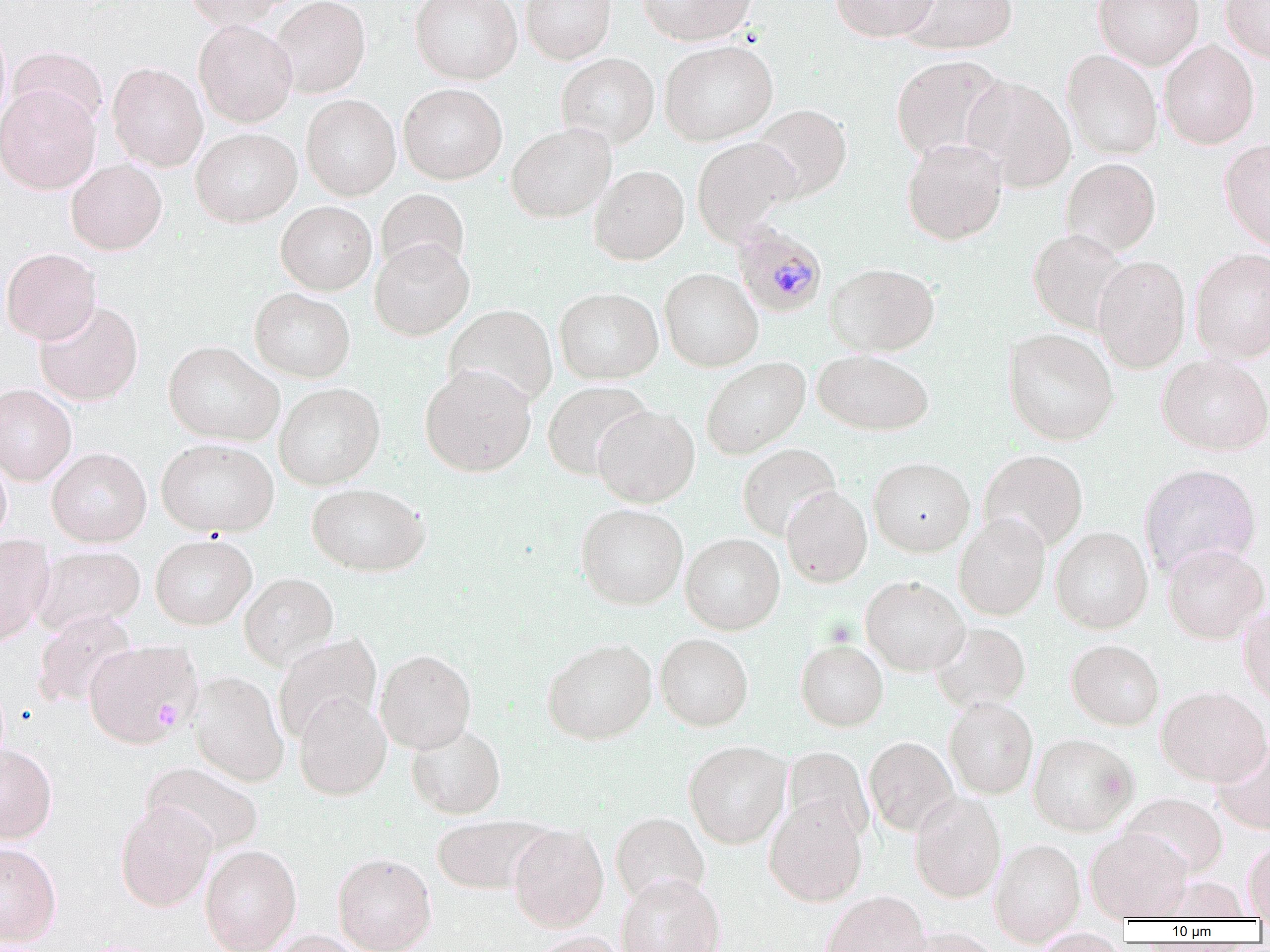

Approximate bounding boxes as (x1,y1)-(x2,y2) corner pairs in pixels. Plasmodium malariae-infected red blood cell locations: (731,221)-(828,319). Platelet locations: (156,700)-(182,732). Uninfected red blood cell locations: (184,0)-(297,28), (270,0)-(371,98), (410,0)-(522,84), (520,0)-(616,63), (638,0)-(758,45), (831,0)-(939,42), (1093,0)-(1204,69), (1220,0)-(1270,63), (898,1)-(1018,54), (194,19)-(297,127), (0,23)-(11,127), (659,39)-(778,146), (1159,39)-(1260,149), (9,47)-(109,131), (1061,49)-(1162,160), (556,52)-(659,147), (891,54)-(1007,162), (107,62)-(208,171), (962,75)-(1076,192), (398,83)-(507,185), (0,85)-(100,194), (301,94)-(401,201), (751,104)-(851,202), (506,123)-(616,222), (191,128)-(302,227), (692,137)-(799,242), (902,138)-(1008,245), (1219,138)-(1270,250), (1061,157)-(1161,256), (66,159)-(166,255), (589,165)-(689,265), (376,188)-(469,277), (276,201)-(377,295), (1028,229)-(1131,334), (370,238)-(474,340), (1,247)-(101,344), (1189,248)-(1270,363), (1092,255)-(1190,373), (825,262)-(940,356), (659,268)-(763,372), (250,287)-(355,382), (554,287)-(663,384), (34,301)-(143,406), (444,304)-(557,408), (1003,329)-(1119,445), (163,340)-(284,446), (813,349)-(933,436), (1157,353)-(1270,456), (701,356)-(810,458), (420,363)-(536,476), (542,380)-(651,479), (274,382)-(385,489), (0,384)-(77,485), (592,405)-(700,507), (156,437)-(279,537), (737,443)-(841,540), (47,447)-(151,547), (979,449)-(1088,553), (0,455)-(11,546), (868,456)-(975,556), (1139,464)-(1261,578), (307,482)-(431,576), (782,486)-(872,587), (575,503)-(688,609), (953,513)-(1051,620), (1050,526)-(1153,633), (681,532)-(785,634), (0,534)-(56,645), (150,535)-(256,629), (1162,542)-(1269,643), (32,544)-(145,635), (240,572)-(338,670), (861,576)-(970,676), (1237,602)-(1270,705), (32,609)-(138,709), (930,622)-(1031,713), (272,632)-(382,745), (655,632)-(754,731), (83,638)-(202,749), (542,638)-(657,744), (795,639)-(888,731), (1067,639)-(1164,730), (375,649)-(476,754), (188,671)-(288,787), (1157,685)-(1270,786), (293,693)-(392,800), (944,697)-(1038,798), (406,722)-(506,819), (1028,733)-(1138,836), (864,736)-(959,836), (1213,740)-(1270,834), (684,741)-(791,848), (0,743)-(57,843), (782,746)-(874,844), (142,761)-(264,856), (909,791)-(1006,903), (1119,792)-(1228,880), (764,797)-(868,906), (115,801)-(217,912), (611,812)-(710,906), (430,815)-(551,894), (509,823)-(609,932), (1086,828)-(1192,921), (989,838)-(1086,946), (1244,840)-(1270,919), (0,842)-(61,946), (200,844)-(302,952), (332,852)-(437,952), (616,873)-(725,952), (821,890)-(932,952), (903,927)-(1005,952), (1030,928)-(1128,952), (265,930)-(366,952), (526,931)-(631,952). Slide-level diagnosis: Plasmodium malariae. Thin blood film. Captured at 1000x magnification. One field of a larger specimen. Image is 1270×952 pixels. Optical microscopy.